Assess this cell for malaria.
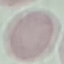

It is uninfected.

{
  "preparation": "thin blood smear",
  "capture": "smartphone camera at the microscope eyepiece",
  "stain": "Giemsa",
  "image_type": "cell patch, automatically extracted from a larger field of view and resized to 64 × 64 pixels"
}